Name the cell type shown.
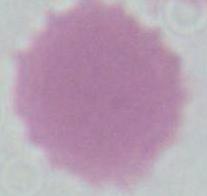
An erythrocyte.

{
  "magnification": "1000x",
  "modality": "photomicrograph"
}